Report the malaria status of this cell.
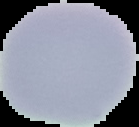
Uninfected.

image type = segmented cell region on a black background
image size = 139×127 pixels
preparation = thin blood film